Give the position of every malaria parasite.
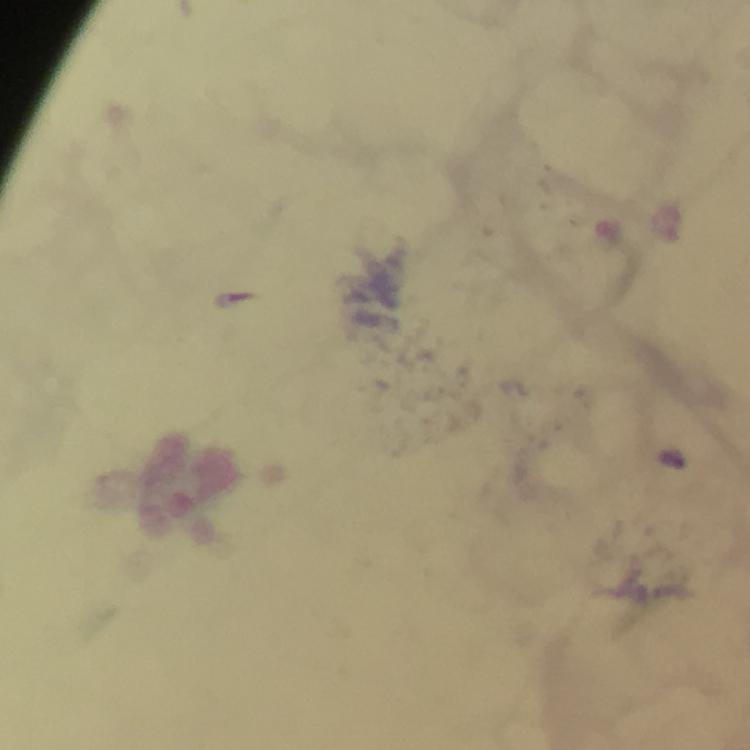
Approximate centers as {x, y} in pixels.
Malaria parasites: {674, 459}.

At 100x magnification. Immersion oil was used. Image is 750×750 pixels. Smartphone photograph taken through a microscope. Thick blood film. Giemsa stain. From a diagnostic examination for malaria. A crop from one field of view.